Point out each Plasmodium parasite.
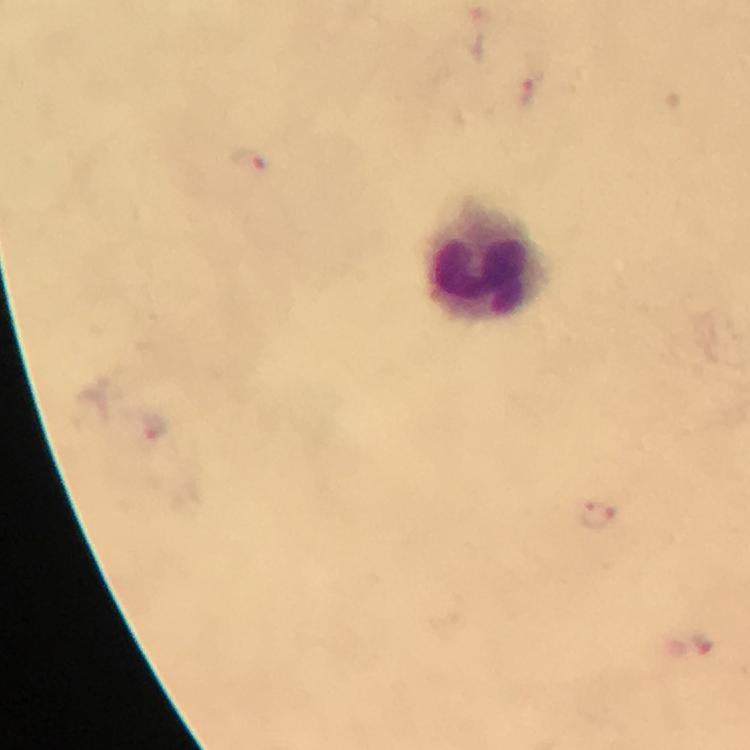

Approximate centers as {x, y} in pixels.
Plasmodium parasites: {529, 90}, {250, 162}, {595, 513}.

Leukocyte locations: {491, 263}. Giemsa stain. Photographed through the microscope with a smartphone camera. A crop from one field of view. Thick blood film. From a diagnostic examination for malaria. At 100x magnification. Immersion oil applied. Image is 750×750 pixels.